Name the cell type shown.
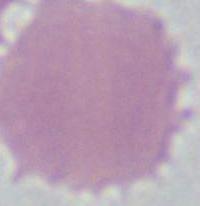

This is an erythrocyte.

magnification: 1000x
modality: micrograph